Locate every uninfected red blood cell.
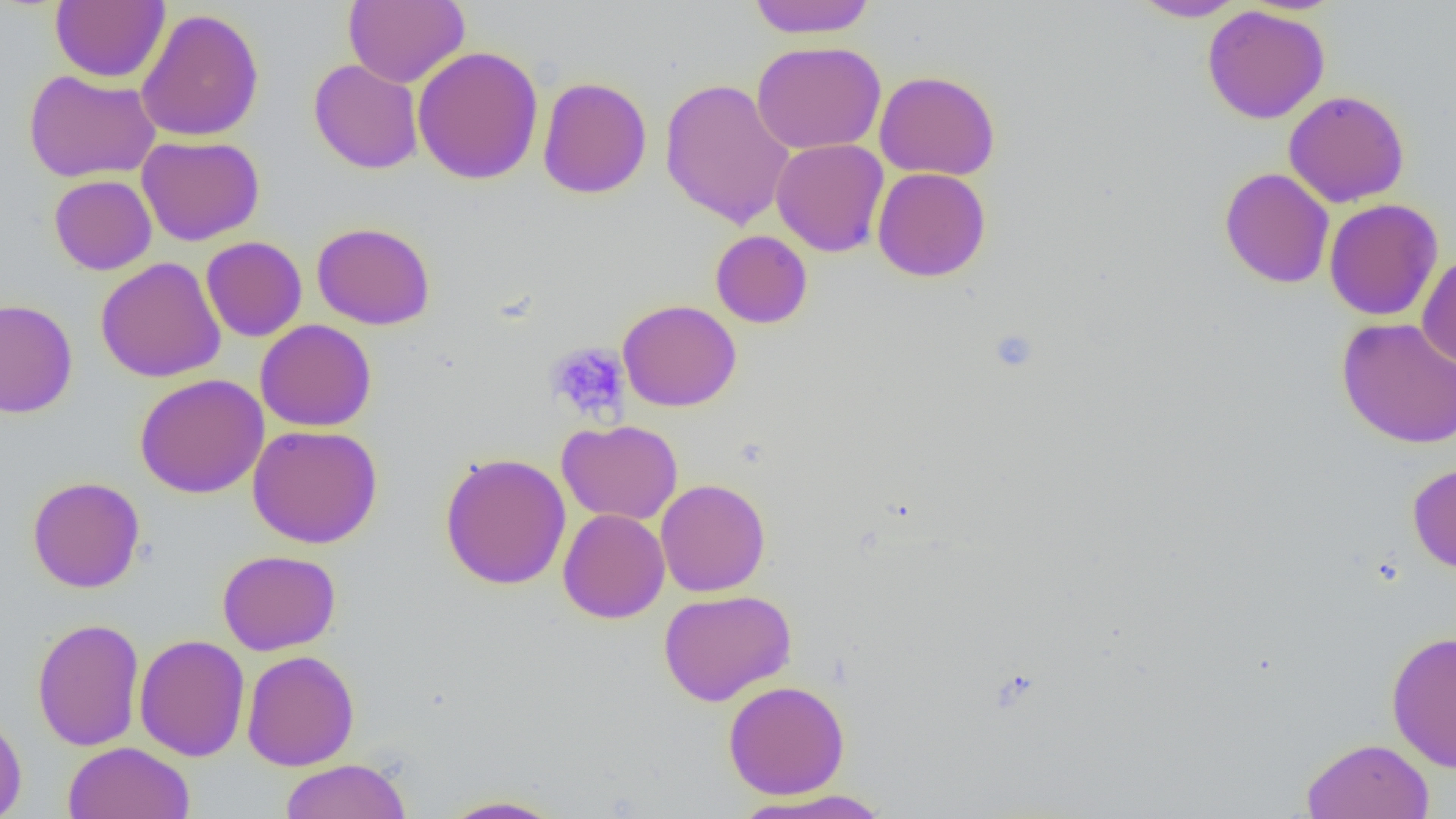
Approximate bounding boxes as (x1, y1, x2, y2) in pixels.
Uninfected red blood cells: (50, 0, 169, 83), (343, 0, 469, 88), (746, 0, 877, 39), (1129, 0, 1248, 22), (1202, 5, 1330, 124), (136, 8, 265, 142), (751, 41, 886, 154), (412, 45, 544, 185), (309, 59, 424, 174), (24, 69, 162, 182), (873, 70, 1001, 181), (537, 76, 652, 199), (659, 77, 795, 230), (1283, 89, 1410, 208), (137, 135, 265, 246), (771, 138, 889, 257), (872, 167, 991, 282), (1219, 167, 1334, 288), (49, 174, 157, 275), (1220, 183, 1441, 300), (1323, 198, 1443, 321), (311, 222, 436, 330), (711, 230, 812, 328), (201, 236, 307, 342), (1416, 253, 1456, 368), (95, 256, 227, 383), (0, 298, 78, 418), (617, 299, 741, 412), (1336, 316, 1456, 449), (255, 319, 376, 432), (135, 373, 269, 498), (557, 419, 683, 525), (248, 424, 383, 548), (439, 452, 572, 590), (1407, 462, 1456, 574), (27, 476, 146, 593), (655, 479, 770, 597), (558, 508, 670, 624), (217, 549, 341, 655), (658, 589, 796, 706), (31, 617, 145, 752), (1386, 630, 1456, 774), (134, 634, 250, 762), (241, 650, 360, 771), (722, 680, 850, 799), (0, 710, 27, 819), (1300, 737, 1435, 819), (62, 741, 196, 819), (279, 758, 413, 819), (731, 789, 892, 818), (435, 794, 569, 818).

Platelet locations: (990, 329, 1038, 373), (545, 341, 631, 423). Slide-level diagnosis: no evidence of blood parasites. One field of a larger specimen. 1000x magnification. Image is 1456×819 pixels. Optical microscopy. Thin blood smear.